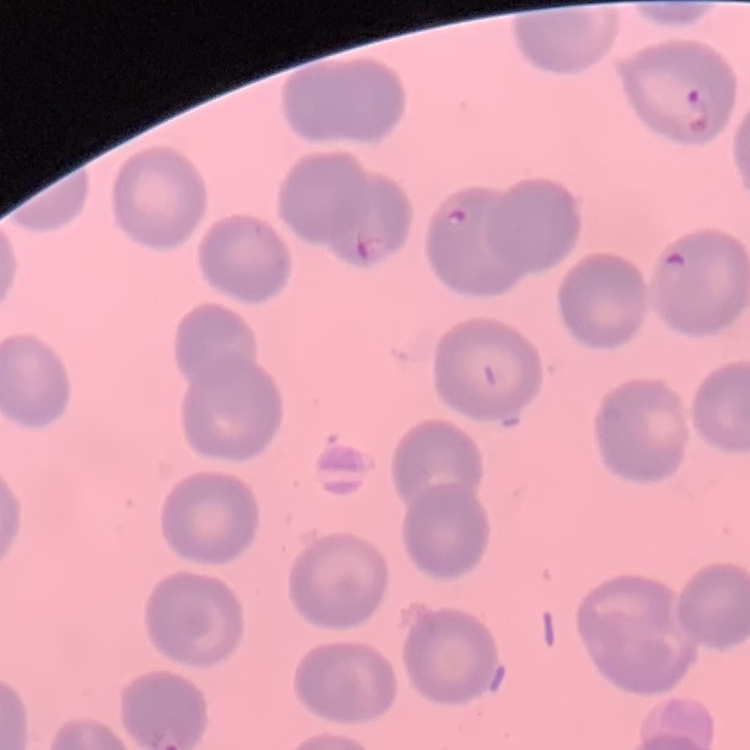 The erythrocytes show no rouleaux formation. Thin blood smear. One tile cut from a larger photomicrograph. Stained with either Field's or Giemsa.